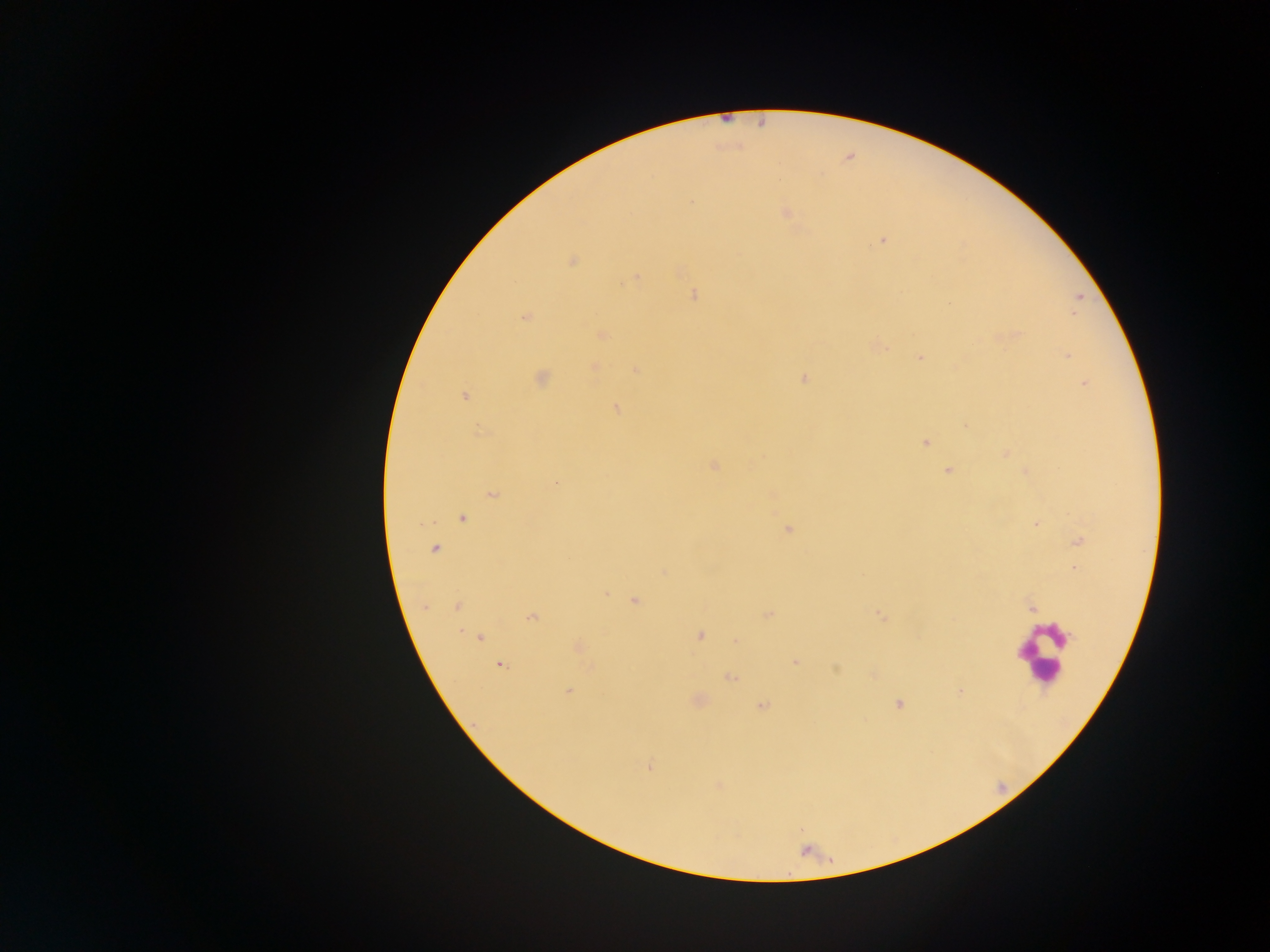
leukocyte_locations: 'approximate centers as {x, y} in pixels: {1044, 652}'
plasmodium_parasite_locations: 'approximate centers as {x, y} in pixels: {786, 213}, {883, 240}, {572, 261}, {636, 279}, {694, 295}, {525, 318}, {602, 335}, {1066, 356}, {920, 358}, {594, 367}, {635, 370}, {541, 378}, {804, 379}, {1084, 383}, {464, 397}, {615, 408}, {480, 433}, {925, 443}, {1006, 454}, {714, 465}, {947, 470}, {556, 483}, {492, 493}, {462, 518}, {420, 523}, {1035, 524}, {788, 529}, {1080, 541}, {434, 549}, {663, 571}, {605, 594}, {634, 601}, {424, 606}, {456, 606}, {1031, 609}, {769, 614}, {880, 616}, {531, 618}, {701, 635}, {479, 637}, {735, 641}, {578, 646}, {796, 661}, {500, 665}, {591, 667}, {836, 668}, {730, 677}, {568, 691}, {960, 692}, {899, 704}, {762, 706}, {650, 766}, {718, 786}'
country: Ghana
capture: mobile-phone photograph through a microscope
field_of_view: single
image_size: 1270×952 pixels
preparation: thick blood film